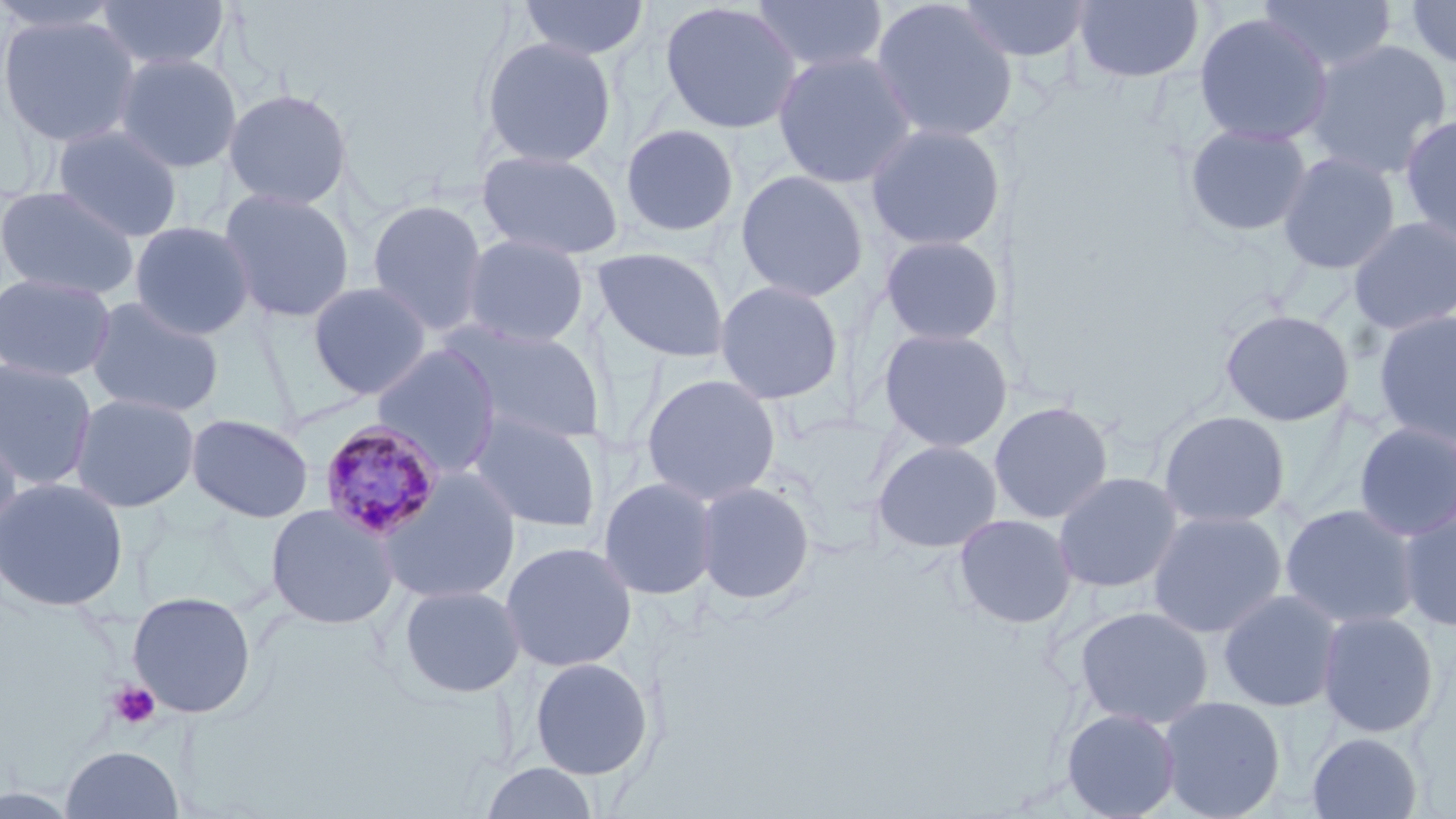

Summary:
  - Coordinate format: approximate bounding boxes as (x1,y1)-(x2,y2) corner pairs in pixels
  - Platelet locations: (107,679)-(162,731)
  - Plasmodium malariae-infected red blood cell locations: (318,419)-(446,541)
  - Uninfected red blood cell locations: (0,0)-(125,35), (95,0)-(230,72), (518,0)-(650,61), (749,0)-(889,75), (870,0)-(1019,144), (955,0)-(1092,63), (1073,0)-(1205,85), (1257,0)-(1398,75), (1403,0)-(1456,71), (658,1)-(803,135), (1193,11)-(1334,148), (0,12)-(143,149), (479,36)-(618,169), (1301,39)-(1453,182), (772,49)-(918,189), (113,52)-(243,173), (222,87)-(353,211), (1399,113)-(1456,246), (864,121)-(1007,252), (619,123)-(740,238), (1183,123)-(1313,237), (52,124)-(184,242), (475,148)-(625,261), (1277,151)-(1401,275), (734,169)-(870,303), (0,184)-(139,301), (218,187)-(356,324), (366,198)-(490,336), (1347,216)-(1456,335), (127,220)-(256,341), (461,233)-(590,348), (878,234)-(1006,346), (592,247)-(730,362), (0,272)-(117,383), (713,279)-(845,405), (307,281)-(432,401), (84,296)-(225,418), (1219,309)-(1355,426), (1374,310)-(1456,447), (446,324)-(604,447), (877,327)-(1010,453), (370,345)-(502,477), (0,358)-(98,491), (640,373)-(782,506), (69,392)-(201,513), (989,400)-(1115,525), (466,409)-(602,534), (1157,410)-(1291,529), (185,413)-(315,523), (1353,421)-(1456,541), (0,427)-(24,551), (870,439)-(1003,554), (375,469)-(522,605), (1052,471)-(1183,593), (597,476)-(719,601), (0,477)-(129,612), (694,480)-(816,605), (265,503)-(400,630), (1279,503)-(1422,630), (1397,503)-(1456,632), (1147,510)-(1288,638), (953,513)-(1078,629), (499,541)-(638,673), (398,583)-(526,699), (1217,588)-(1344,712), (127,590)-(257,719), (1074,605)-(1214,728), (1317,610)-(1440,738), (529,657)-(654,780), (1158,695)-(1286,819), (1060,707)-(1182,819), (1307,731)-(1423,819), (60,745)-(185,819), (478,762)-(602,819)
  - Slide-level diagnosis: Plasmodium malariae
  - Image size: 1456×819 pixels
  - Field of view: single
  - Magnification: 1000x
  - Preparation: thin blood film
  - Modality: optical microscopy
  - Stain: May-Grünwald-Giemsa